Locate every uninfected red blood cell.
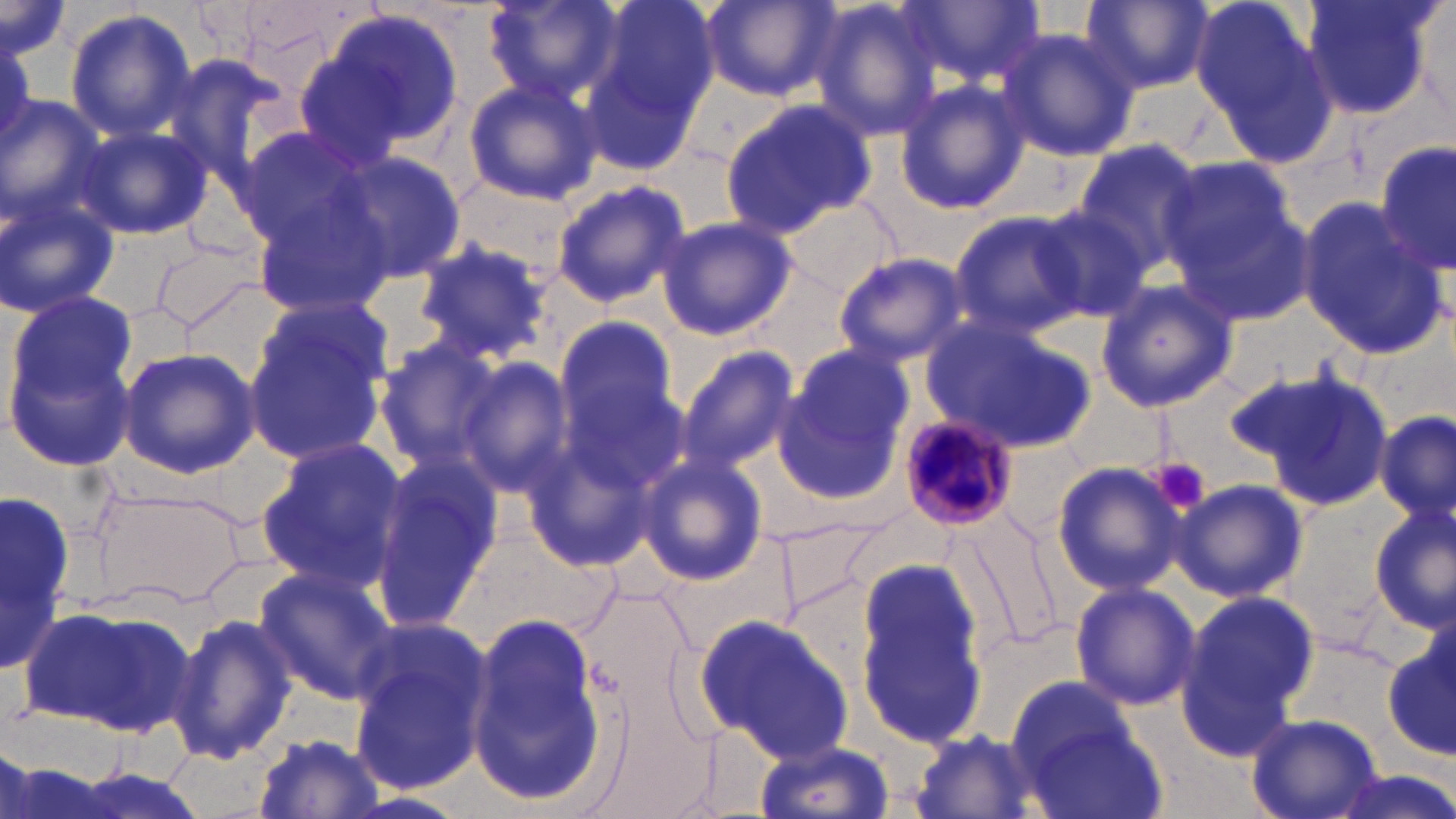
Approximate bounding boxes as (x1, y1, x2, y2) in pixels.
Uninfected red blood cells: (480, 0, 624, 110), (578, 0, 720, 172), (701, 0, 843, 101), (809, 0, 950, 142), (902, 0, 1043, 92), (1081, 0, 1214, 95), (1191, 0, 1338, 163), (1300, 0, 1440, 122), (1, 2, 70, 64), (64, 8, 197, 141), (308, 8, 466, 156), (995, 26, 1140, 163), (462, 76, 604, 206), (895, 79, 1030, 216), (0, 94, 110, 237), (718, 96, 881, 238), (72, 120, 213, 241), (231, 124, 380, 252), (1072, 139, 1206, 273), (1377, 140, 1454, 278), (334, 152, 468, 281), (1158, 156, 1317, 323), (550, 178, 692, 307), (0, 189, 120, 320), (249, 191, 396, 317), (778, 193, 900, 298), (1033, 200, 1160, 323), (1296, 201, 1444, 358), (948, 207, 1093, 337), (656, 215, 796, 341), (409, 237, 555, 365), (151, 239, 265, 329), (833, 251, 968, 367), (1094, 278, 1239, 414), (6, 291, 142, 467), (240, 305, 394, 464), (921, 314, 1096, 456), (551, 316, 684, 453), (374, 337, 510, 471), (677, 345, 800, 473), (117, 346, 261, 477), (777, 346, 913, 498), (460, 354, 575, 498), (1247, 367, 1397, 512), (560, 376, 689, 496), (1377, 408, 1454, 526), (254, 438, 410, 593), (637, 453, 768, 586), (369, 454, 508, 629), (1049, 460, 1185, 596), (1171, 478, 1308, 603), (85, 483, 246, 607), (0, 491, 77, 679), (1369, 504, 1456, 630), (961, 510, 1062, 652), (852, 564, 990, 745), (252, 565, 396, 705), (1068, 581, 1201, 712), (1175, 588, 1318, 759), (23, 603, 198, 738), (467, 609, 608, 810), (168, 612, 298, 766), (697, 614, 855, 762), (348, 621, 491, 796), (1381, 632, 1456, 758), (1005, 675, 1139, 786), (1246, 713, 1383, 819), (1018, 715, 1167, 819), (905, 726, 1043, 819), (252, 733, 384, 818), (754, 738, 895, 819), (1324, 771, 1456, 819).

slide_level_diagnosis: Plasmodium malariae
platelet_locations: 'approximate bounding boxes as (x1, y1, x2, y2) in pixels: (1154, 458, 1212, 515)'
field_of_view: one of a larger specimen
plasmodium_malariae_infected_red_blood_cell_locations: 'approximate bounding boxes as (x1, y1, x2, y2) in pixels: (896, 411, 1023, 529)'
modality: light microscopy
image_size: 1456×819 pixels
preparation: thin blood film
magnification: 1000x
stain: May-Grünwald-Giemsa